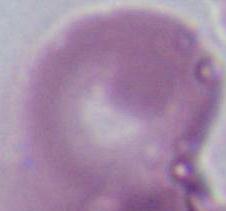
A red blood cell is shown. Captured at 1000x magnification. Photomicrograph.